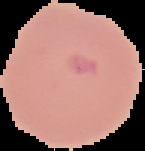

image type = cell region segmented out of the field of view; surrounding area masked to black
image size = 145×151 pixels
malaria status = parasitized
preparation = thin blood film